Find the cells and give the type of each one.
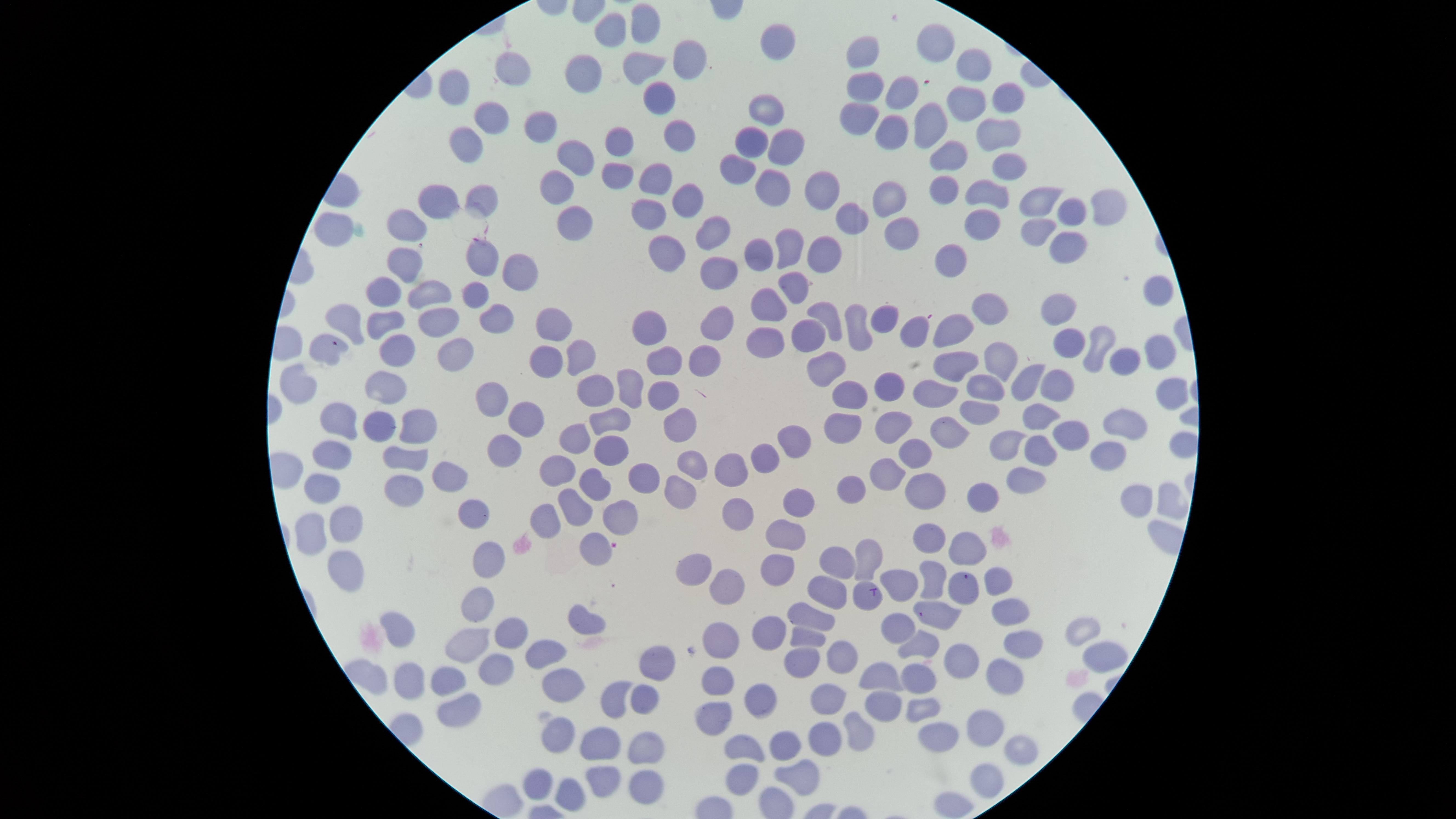

No parasitized red blood cells identified.
Approximate marker points, in pixels from the top-left corner.
Uninfected red blood cells: (x=648, y=20), (x=609, y=30), (x=943, y=37), (x=776, y=44), (x=859, y=48), (x=692, y=68), (x=511, y=69), (x=638, y=71), (x=969, y=71), (x=581, y=73), (x=452, y=79), (x=871, y=87), (x=1011, y=94), (x=900, y=95), (x=654, y=96), (x=969, y=98), (x=765, y=107), (x=489, y=113), (x=858, y=117), (x=934, y=117), (x=536, y=124), (x=674, y=128), (x=893, y=132), (x=989, y=133), (x=625, y=136), (x=786, y=139), (x=756, y=140), (x=465, y=146), (x=573, y=149), (x=944, y=154), (x=1010, y=166), (x=739, y=169), (x=654, y=171), (x=618, y=173), (x=777, y=180), (x=955, y=185), (x=551, y=186), (x=825, y=192), (x=995, y=193), (x=483, y=198), (x=896, y=198), (x=448, y=199), (x=684, y=199), (x=1047, y=203), (x=1105, y=205), (x=1069, y=208), (x=652, y=212), (x=983, y=214), (x=574, y=220), (x=409, y=222), (x=853, y=222), (x=340, y=223), (x=1035, y=227), (x=902, y=228), (x=707, y=237), (x=786, y=244), (x=1064, y=247), (x=472, y=250), (x=826, y=254), (x=663, y=255), (x=958, y=255), (x=760, y=257), (x=401, y=259), (x=715, y=265), (x=517, y=270), (x=393, y=285), (x=794, y=292), (x=481, y=293), (x=434, y=296), (x=1161, y=298), (x=762, y=305), (x=1054, y=308), (x=990, y=310), (x=346, y=315), (x=545, y=315), (x=383, y=316), (x=489, y=316), (x=829, y=316), (x=888, y=319), (x=639, y=321), (x=854, y=323), (x=438, y=324), (x=714, y=325), (x=918, y=326), (x=950, y=330), (x=815, y=334), (x=1072, y=342), (x=333, y=343), (x=1153, y=343), (x=1102, y=345), (x=397, y=346), (x=766, y=346), (x=577, y=348), (x=1000, y=353), (x=458, y=354), (x=703, y=354), (x=957, y=361), (x=1125, y=362), (x=543, y=363), (x=667, y=364), (x=826, y=368), (x=636, y=379), (x=984, y=379), (x=888, y=380), (x=1025, y=381), (x=301, y=384), (x=1051, y=384), (x=387, y=387), (x=845, y=390), (x=931, y=390), (x=593, y=391), (x=661, y=395), (x=491, y=397), (x=339, y=413), (x=1041, y=413), (x=525, y=416), (x=896, y=417), (x=603, y=419), (x=674, y=421), (x=1123, y=422), (x=367, y=423), (x=416, y=423), (x=840, y=424), (x=1073, y=430), (x=949, y=431), (x=793, y=435), (x=574, y=440), (x=1010, y=440), (x=506, y=449), (x=609, y=449), (x=1041, y=452), (x=915, y=453), (x=1106, y=455), (x=400, y=456), (x=327, y=457), (x=763, y=459), (x=691, y=460), (x=727, y=462), (x=559, y=470), (x=883, y=471), (x=639, y=473), (x=1023, y=474), (x=448, y=476), (x=593, y=480), (x=324, y=487), (x=924, y=487), (x=675, y=490), (x=404, y=491), (x=851, y=492), (x=983, y=493), (x=1137, y=497), (x=797, y=504), (x=573, y=506), (x=735, y=511), (x=469, y=514), (x=544, y=516), (x=616, y=519), (x=345, y=525), (x=305, y=534), (x=789, y=536), (x=930, y=536), (x=590, y=544), (x=968, y=549), (x=485, y=555), (x=872, y=555), (x=840, y=563), (x=340, y=566), (x=698, y=567), (x=775, y=571), (x=931, y=576), (x=999, y=576), (x=904, y=581), (x=731, y=583), (x=959, y=584), (x=832, y=587), (x=865, y=593), (x=474, y=601), (x=1008, y=607), (x=942, y=615), (x=815, y=619), (x=404, y=620), (x=588, y=623), (x=901, y=624), (x=1086, y=627), (x=513, y=629), (x=720, y=630), (x=766, y=630), (x=809, y=630), (x=917, y=640), (x=471, y=642), (x=1019, y=642), (x=839, y=650), (x=804, y=651), (x=959, y=651), (x=541, y=652), (x=1098, y=658), (x=493, y=660), (x=649, y=661), (x=916, y=671), (x=368, y=673), (x=447, y=676), (x=885, y=676), (x=407, y=679), (x=718, y=680), (x=1001, y=680), (x=560, y=682), (x=645, y=693), (x=616, y=694), (x=828, y=698), (x=756, y=702), (x=453, y=704), (x=884, y=705), (x=920, y=705), (x=714, y=713), (x=986, y=724), (x=854, y=730), (x=556, y=731), (x=825, y=734), (x=943, y=734), (x=788, y=737), (x=640, y=741), (x=600, y=744), (x=739, y=746), (x=1017, y=750), (x=795, y=766), (x=535, y=774), (x=599, y=778), (x=980, y=779), (x=737, y=781), (x=643, y=784), (x=569, y=791).
No white blood cells identified.

Summary:
  - Capture: smartphone photograph through the microscope eyepiece
  - Preparation: thin blood smear
  - Stain: Giemsa
  - Image size: 1456×819 pixels
  - Field of view: single
  - Visible region: circular